State which cell type is depicted.
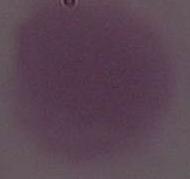

This is an erythrocyte.

magnification = 1000x
modality = photomicrograph